Give the position of every malaria parasite.
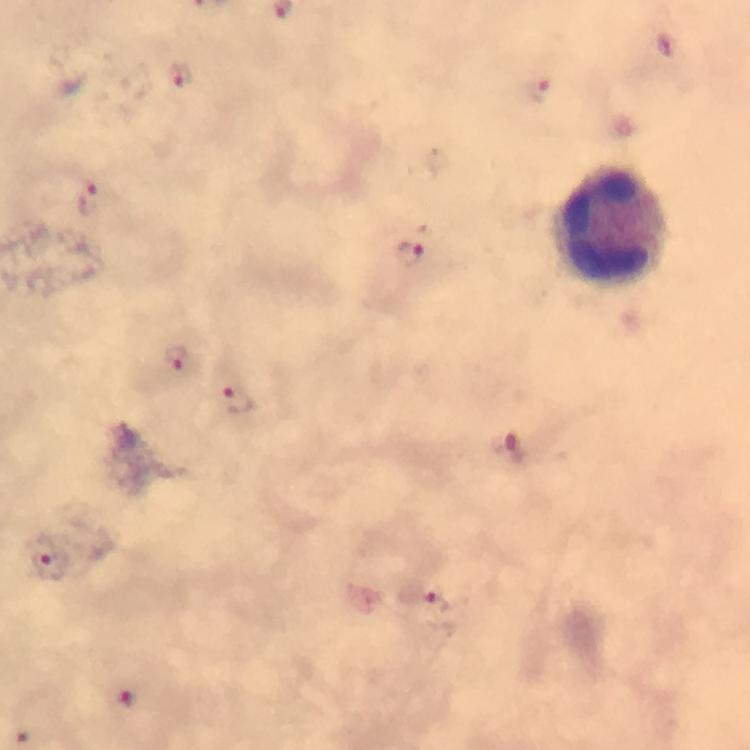
Approximate centers as (x, y) in pixels.
Malaria parasites: (666, 46), (180, 75), (535, 88), (90, 199), (414, 257), (175, 357), (237, 400), (510, 452), (47, 561), (433, 603), (127, 698), (24, 734).

Leukocyte locations: (610, 226). Cropped region of a single field of view. Thick blood smear. 100x magnification. Photographed with a smartphone mounted on the microscope. From a malaria diagnostic workup. Giemsa-stained preparation. Image is 750×750 pixels. Immersion oil applied.